Outline each blood parasite and name the species.
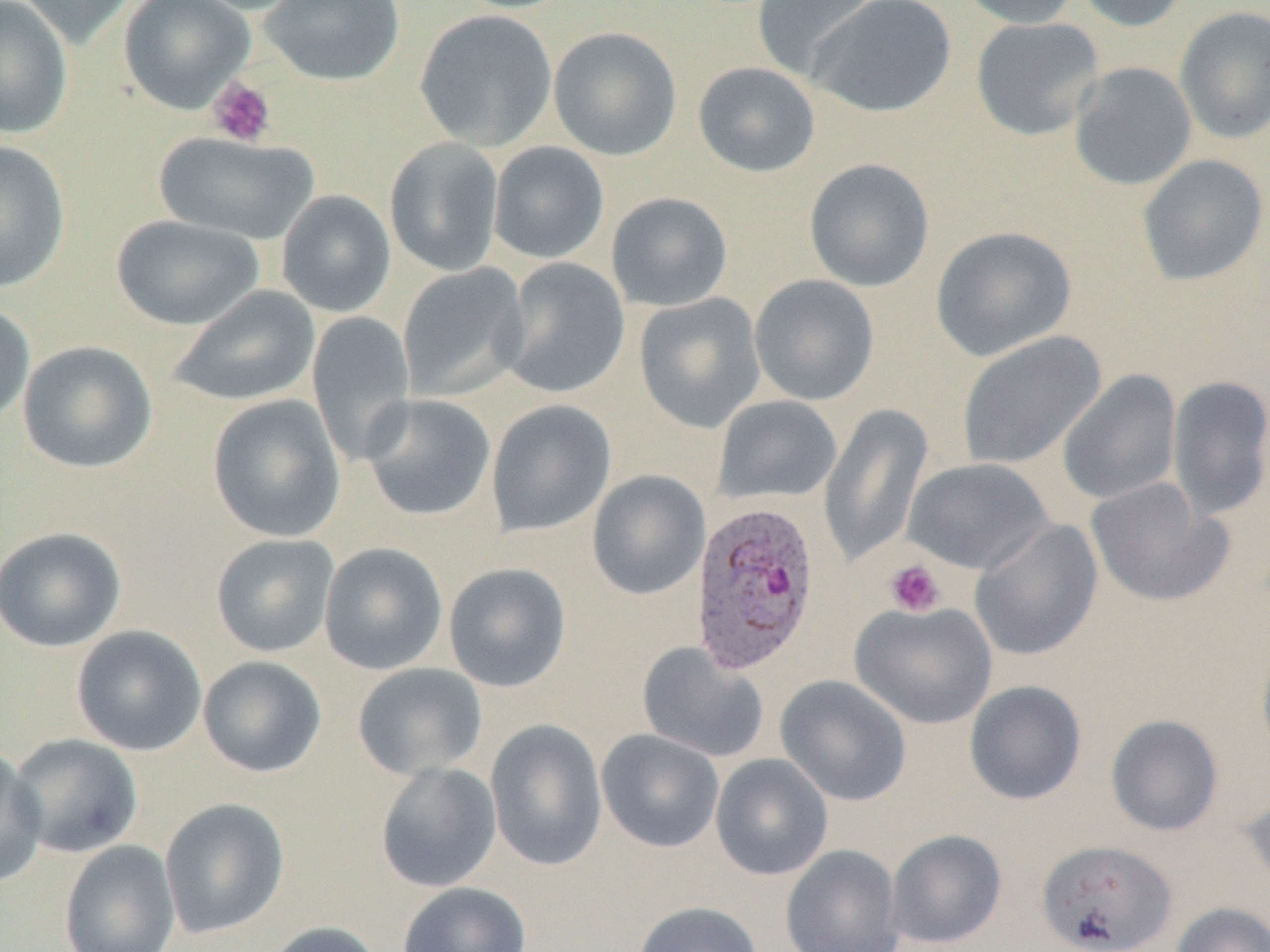

Approximate bounding boxes as (x1,y1)-(x2,y2) corner pairs in pixels.
Plasmodium ovale-infected red blood cells: (689,500)-(821,677).
No Plasmodium falciparum, Plasmodium malariae, Plasmodium vivax, Babesia divergens, or Trypanosoma brucei observed.

slide-level diagnosis = Plasmodium ovale
platelet locations = approximate bounding boxes as (x1,y1)-(x2,y2) corner pairs in pixels: (207,77)-(276,147), (884,559)-(946,617)
field of view = one of a larger specimen
image size = 1270×952 pixels
preparation = thin blood smear
uninfected red blood cell locations = approximate bounding boxes as (x1,y1)-(x2,y2) corner pairs in pixels: (0,0)-(73,139), (14,0)-(138,50), (118,0)-(255,114), (179,0)-(312,15), (259,0)-(405,86), (450,0)-(577,14), (752,0)-(879,83), (809,0)-(956,118), (956,0)-(1080,28), (1071,0)-(1192,33), (1174,6)-(1270,144), (414,9)-(558,151), (970,17)-(1104,141), (548,26)-(682,161), (693,62)-(820,177), (1068,62)-(1197,190), (153,132)-(319,245), (384,137)-(504,277), (0,140)-(70,293), (488,141)-(609,264), (1137,154)-(1269,286), (804,158)-(935,292), (276,190)-(396,317), (606,192)-(733,312), (111,214)-(264,330), (931,226)-(1077,362), (498,258)-(631,399), (397,263)-(531,403), (749,274)-(880,405), (167,286)-(320,407), (634,293)-(766,433), (0,302)-(35,428), (307,311)-(416,466), (956,331)-(1106,470), (17,340)-(158,474), (1057,370)-(1182,505), (1167,375)-(1270,522), (207,394)-(346,543), (360,394)-(496,522), (712,395)-(842,506), (486,399)-(616,538), (818,402)-(934,568), (903,458)-(1053,575), (587,470)-(711,600), (1085,478)-(1233,608), (970,519)-(1103,661), (0,526)-(127,652), (210,533)-(340,658), (319,542)-(448,675), (443,562)-(572,692), (850,601)-(998,729), (71,625)-(207,756), (1256,635)-(1270,764), (637,642)-(769,763), (198,655)-(327,778), (352,662)-(488,779), (775,675)-(912,806), (964,680)-(1087,805), (1105,714)-(1224,837), (486,719)-(607,872), (596,729)-(725,853), (7,733)-(143,859), (0,746)-(47,887), (710,753)-(833,881), (375,762)-(502,893), (1242,786)-(1270,893), (160,798)-(290,939), (885,829)-(1007,948), (1035,839)-(1177,952), (59,840)-(181,952), (780,845)-(905,952), (397,882)-(532,952), (633,901)-(763,952), (1170,902)-(1270,952), (259,920)-(385,952)
magnification = 1000x
modality = optical microscopy